Give the position of every Plasmodium parasite visible.
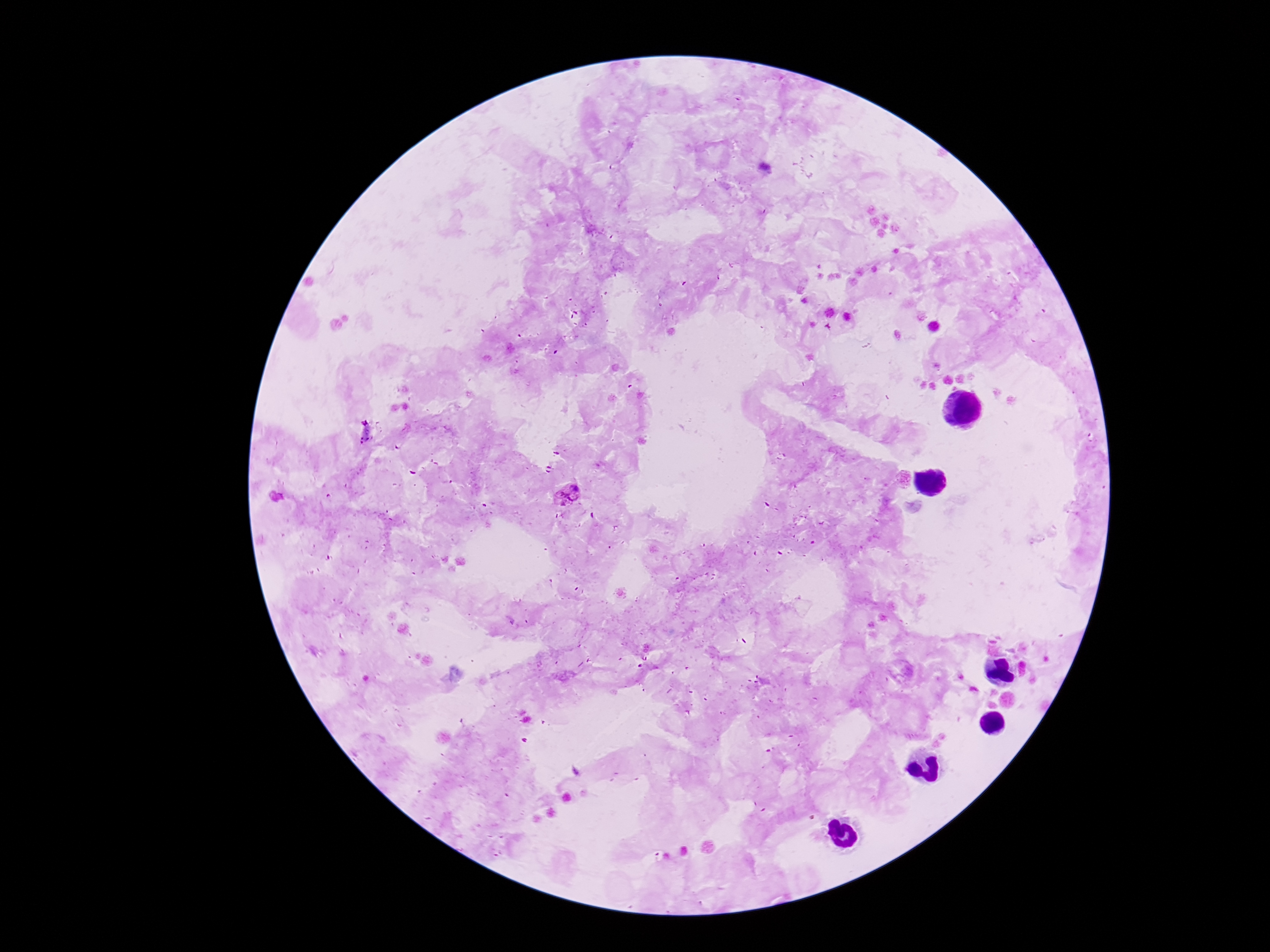

Approximate centers as {x, y} in pixels.
Plasmodium parasites: {365, 432}, {567, 494}.

Smartphone photograph taken through the microscope eyepiece. Giemsa-stained preparation. 100x magnification. Patient malaria status: infected. Single field of view. Thick blood film. Image is 1270×952 pixels.